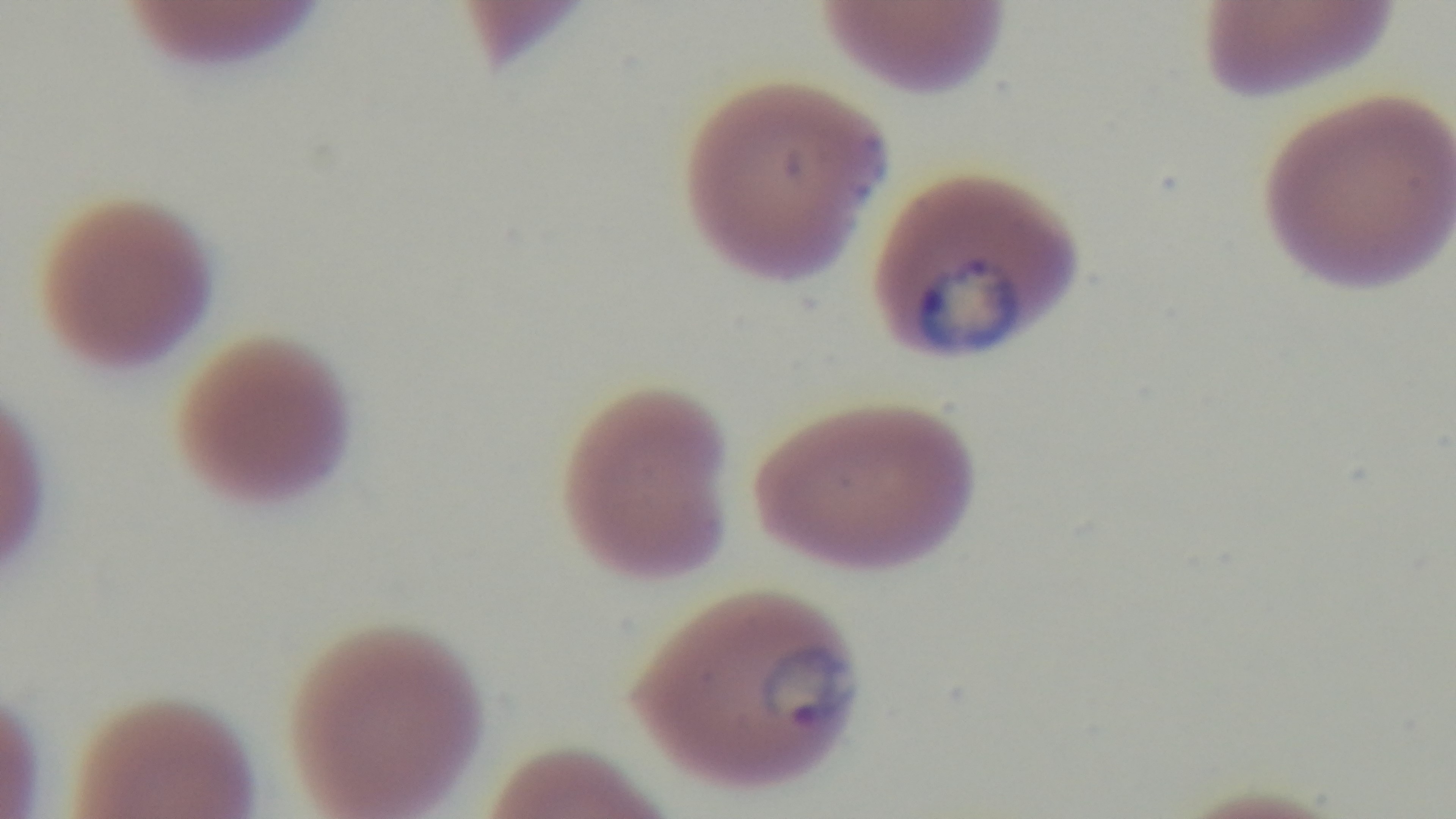

malaria_status: infected
objective: 100x oil immersion
field_of_view: one from the slide
capture: mounted 4K digital camera
stain: Giemsa
modality: light microscopy
preparation: thin smear